Assess the morphology of the red blood cells.
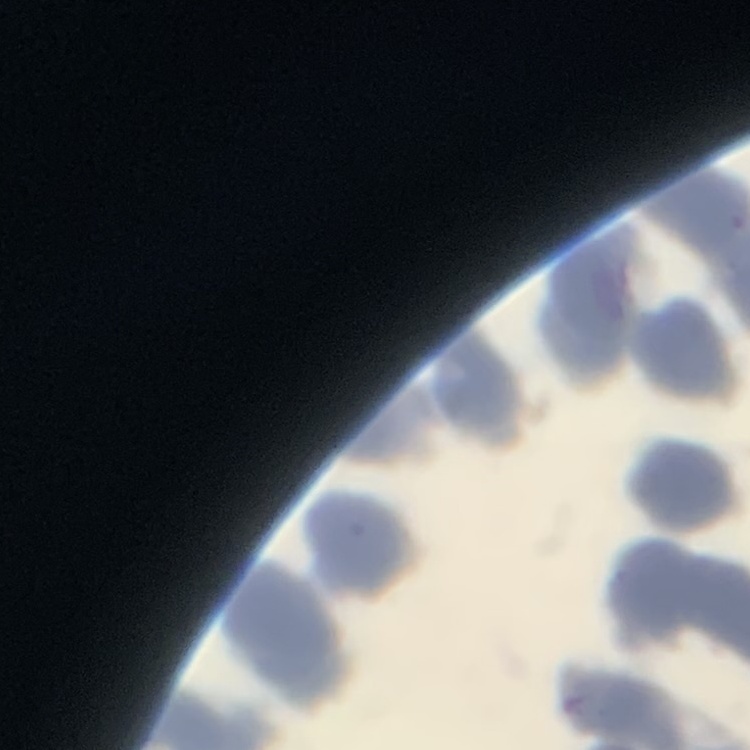

Rouleaux formation.

Summary:
  - Preparation: thin blood film
  - Image type: one tile cut from a larger photomicrograph
  - Stain: Field's or Giemsa